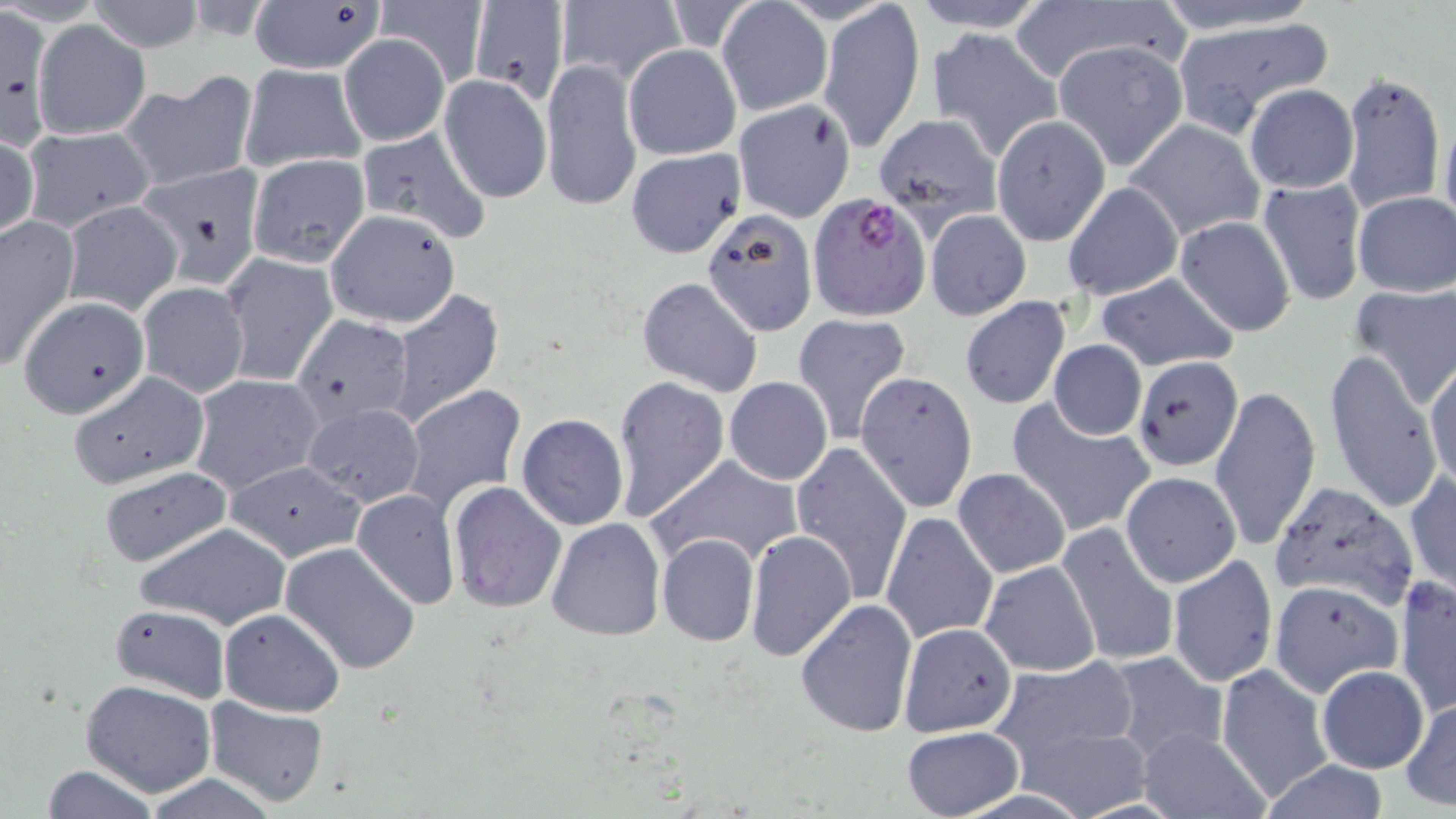

slide-level diagnosis = Plasmodium falciparum
magnification = 1000x
field of view = one of a larger specimen
Plasmodium falciparum-infected red blood cell locations = approximate bounding boxes as (x1, y1, x2, y2) in pixels: (808, 192, 930, 320)
preparation = thin blood film
image size = 1456×819 pixels
uninfected red blood cell locations = approximate bounding boxes as (x1, y1, x2, y2) in pixels: (247, 0, 388, 77), (467, 0, 569, 104), (817, 0, 924, 152), (907, 0, 1051, 32), (1153, 0, 1324, 34), (87, 1, 206, 51), (377, 1, 487, 88), (555, 1, 684, 88), (717, 1, 831, 118), (1020, 4, 1177, 93), (0, 13, 61, 138), (1173, 18, 1335, 139), (32, 20, 150, 139), (924, 26, 1062, 160), (338, 35, 450, 146), (1050, 40, 1189, 172), (623, 44, 741, 160), (541, 58, 641, 212), (561, 58, 731, 193), (237, 63, 367, 172), (1341, 69, 1445, 216), (120, 71, 258, 194), (438, 75, 552, 203), (1244, 84, 1357, 194), (733, 99, 855, 224), (1438, 109, 1455, 238), (871, 113, 1000, 227), (991, 114, 1110, 245), (1125, 118, 1264, 241), (20, 126, 155, 233), (355, 126, 492, 245), (0, 130, 38, 242), (624, 149, 746, 258), (247, 154, 370, 268), (141, 164, 268, 285), (1257, 177, 1367, 307), (1063, 182, 1182, 302), (1352, 191, 1456, 298), (61, 201, 182, 315), (701, 207, 818, 335), (325, 209, 460, 329), (925, 210, 1031, 321), (0, 213, 80, 370), (1175, 216, 1297, 337), (220, 253, 338, 387), (1096, 271, 1238, 371), (636, 276, 764, 397), (136, 281, 249, 397), (1348, 284, 1456, 411), (387, 289, 505, 427), (18, 297, 151, 418), (959, 297, 1070, 409), (292, 314, 415, 426), (792, 314, 913, 443), (1048, 340, 1146, 440), (1323, 349, 1445, 516), (1134, 355, 1244, 471), (1425, 359, 1455, 493), (68, 371, 209, 490), (854, 371, 977, 512), (190, 373, 323, 496), (612, 375, 729, 521), (725, 377, 833, 485), (401, 385, 525, 516), (1210, 385, 1320, 551), (1010, 401, 1154, 538), (300, 402, 424, 510), (516, 412, 630, 531), (789, 440, 913, 602), (647, 453, 802, 570), (227, 459, 365, 562), (99, 468, 234, 567), (952, 469, 1071, 578), (1122, 471, 1240, 586), (1406, 471, 1455, 597), (445, 480, 567, 614), (1269, 480, 1418, 613), (352, 489, 460, 609), (882, 511, 998, 645), (545, 517, 666, 641), (135, 521, 292, 631), (1057, 522, 1178, 669), (743, 528, 857, 664), (656, 533, 758, 646), (281, 542, 422, 674), (1168, 554, 1278, 686), (980, 559, 1101, 676), (1395, 576, 1455, 717), (1270, 580, 1401, 695), (796, 599, 918, 738), (108, 603, 231, 704), (218, 607, 345, 716), (899, 621, 1017, 735), (899, 622, 1019, 738), (1109, 651, 1228, 765), (989, 657, 1144, 771), (1217, 664, 1333, 799), (1315, 666, 1428, 772), (81, 679, 216, 797), (1401, 694, 1456, 811), (204, 697, 330, 808), (1009, 722, 1154, 819), (901, 726, 1025, 819), (1139, 729, 1268, 817), (1258, 759, 1388, 818), (36, 763, 161, 819), (143, 775, 276, 818)
stain = May-Grünwald-Giemsa
modality = light microscopy